Classify this cell by malaria status.
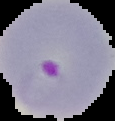
Parasitized.

Summary:
  - Preparation: thin blood smear
  - Image type: segmented cell region on a black background
  - Image size: 115×121 pixels